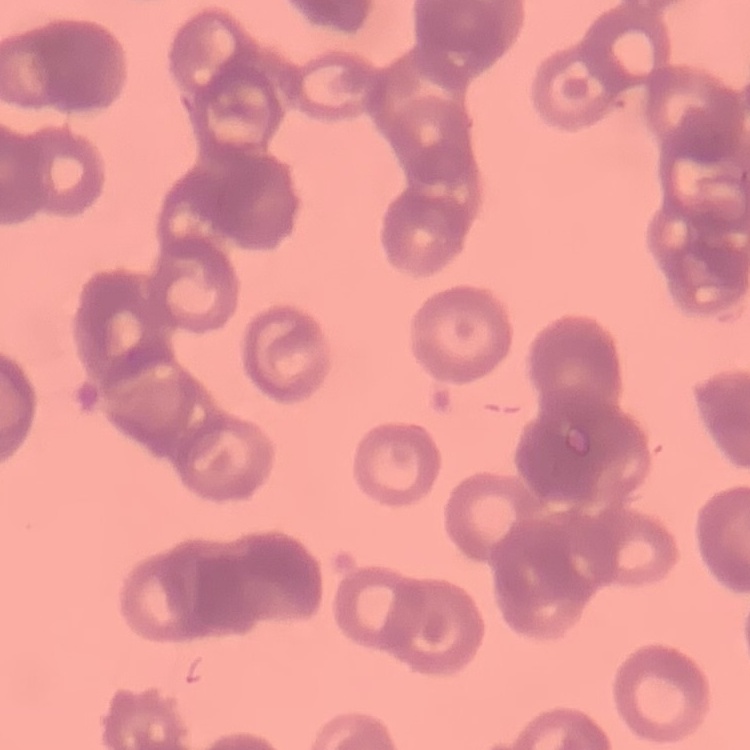

red blood cell morphology = rouleaux formation
preparation = thin blood smear
stain = Field's or Giemsa
image type = square crop of a larger photomicrograph